Name the parasite shown.
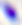
Toxoplasma gondii.

Summary:
  - Magnification: 400x
  - Modality: micrograph